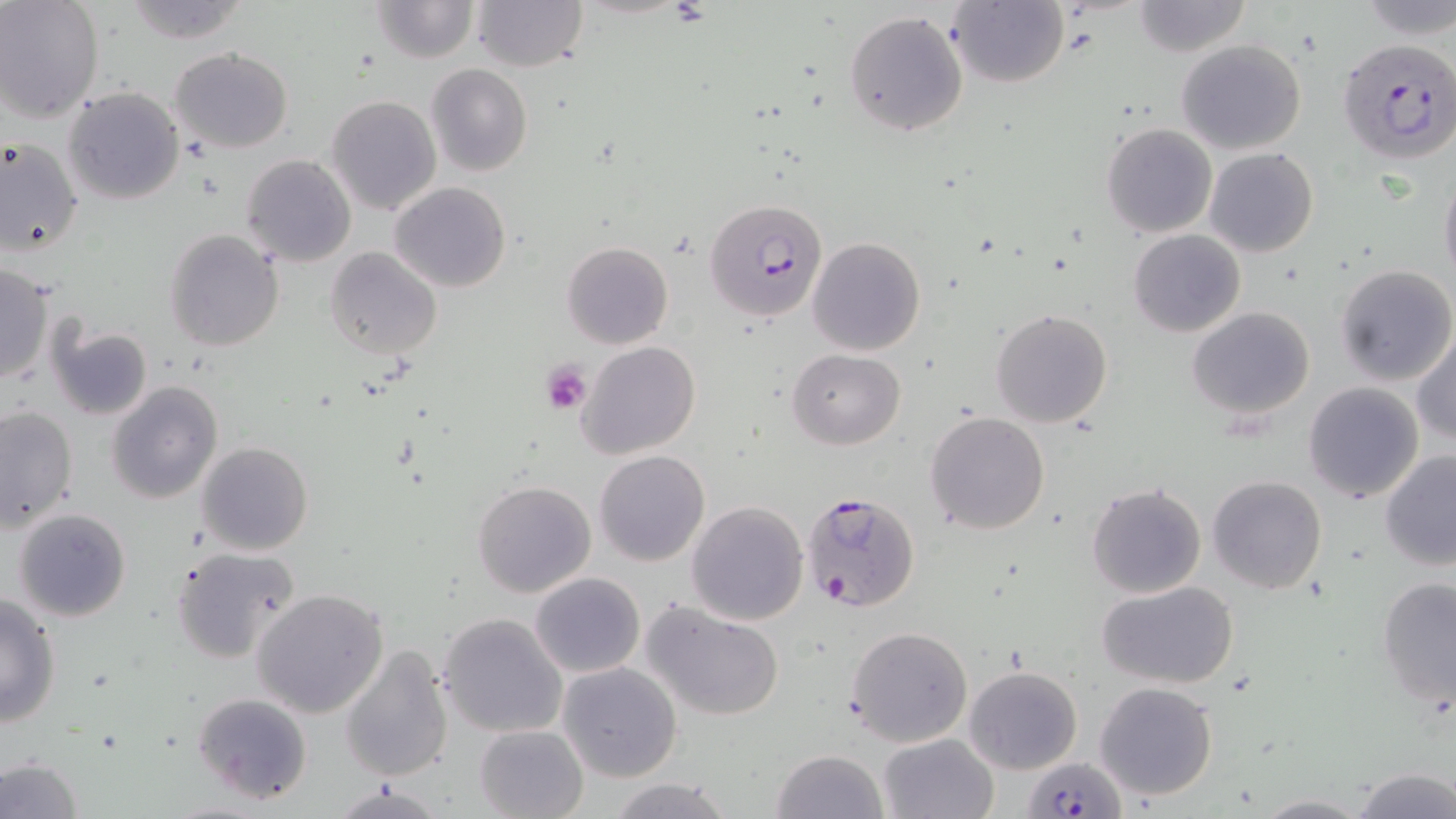

Approximate bounding boxes as (x1,y1)-(x2,y2) corner pairs in pixels. Platelet locations: (542,359)-(593,413). Plasmodium falciparum-infected red blood cell locations: (1337,37)-(1456,163), (705,199)-(828,321), (798,490)-(923,614), (1023,754)-(1122,817). Uninfected red blood cell locations: (121,0)-(253,45), (472,0)-(588,71), (949,0)-(1070,88), (1353,0)-(1455,39), (0,1)-(103,123), (370,1)-(478,64), (1132,1)-(1252,56), (843,9)-(969,138), (1176,39)-(1307,155), (169,47)-(294,152), (426,65)-(532,178), (63,87)-(184,205), (325,95)-(442,215), (1101,123)-(1217,238), (0,137)-(83,259), (1205,147)-(1319,257), (242,155)-(357,268), (1439,168)-(1456,294), (390,180)-(510,293), (1128,229)-(1245,337), (165,230)-(285,351), (807,236)-(925,356), (560,242)-(673,350), (324,247)-(443,360), (1,264)-(54,385), (1334,264)-(1456,386), (1187,307)-(1313,420), (990,308)-(1112,428), (47,321)-(152,421), (1411,331)-(1456,447), (576,341)-(702,461), (788,348)-(905,449), (108,380)-(224,504), (1303,383)-(1423,503), (0,405)-(78,531), (924,411)-(1051,536), (195,441)-(314,555), (594,449)-(709,566), (1379,450)-(1456,571), (1208,474)-(1327,593), (472,480)-(597,598), (1086,483)-(1207,599), (686,500)-(810,625), (12,507)-(131,623), (171,545)-(300,664), (531,572)-(645,677), (1377,576)-(1456,710), (1097,579)-(1240,688), (251,588)-(391,718), (0,592)-(61,727), (643,602)-(787,720), (437,612)-(569,738), (846,625)-(973,748), (339,644)-(455,783), (558,662)-(683,782), (964,666)-(1081,773), (1095,681)-(1219,801), (191,692)-(313,806), (474,724)-(588,818), (878,733)-(998,819), (772,749)-(887,819), (0,756)-(84,818), (1349,768)-(1456,819), (605,777)-(735,819), (332,781)-(445,819), (1252,793)-(1372,817). Slide-level diagnosis: Plasmodium falciparum. Thin blood film. Optical microscopy. One field of a larger specimen. Captured at 1000x magnification. May-Grünwald-Giemsa stain. Image is 1456×819 pixels.